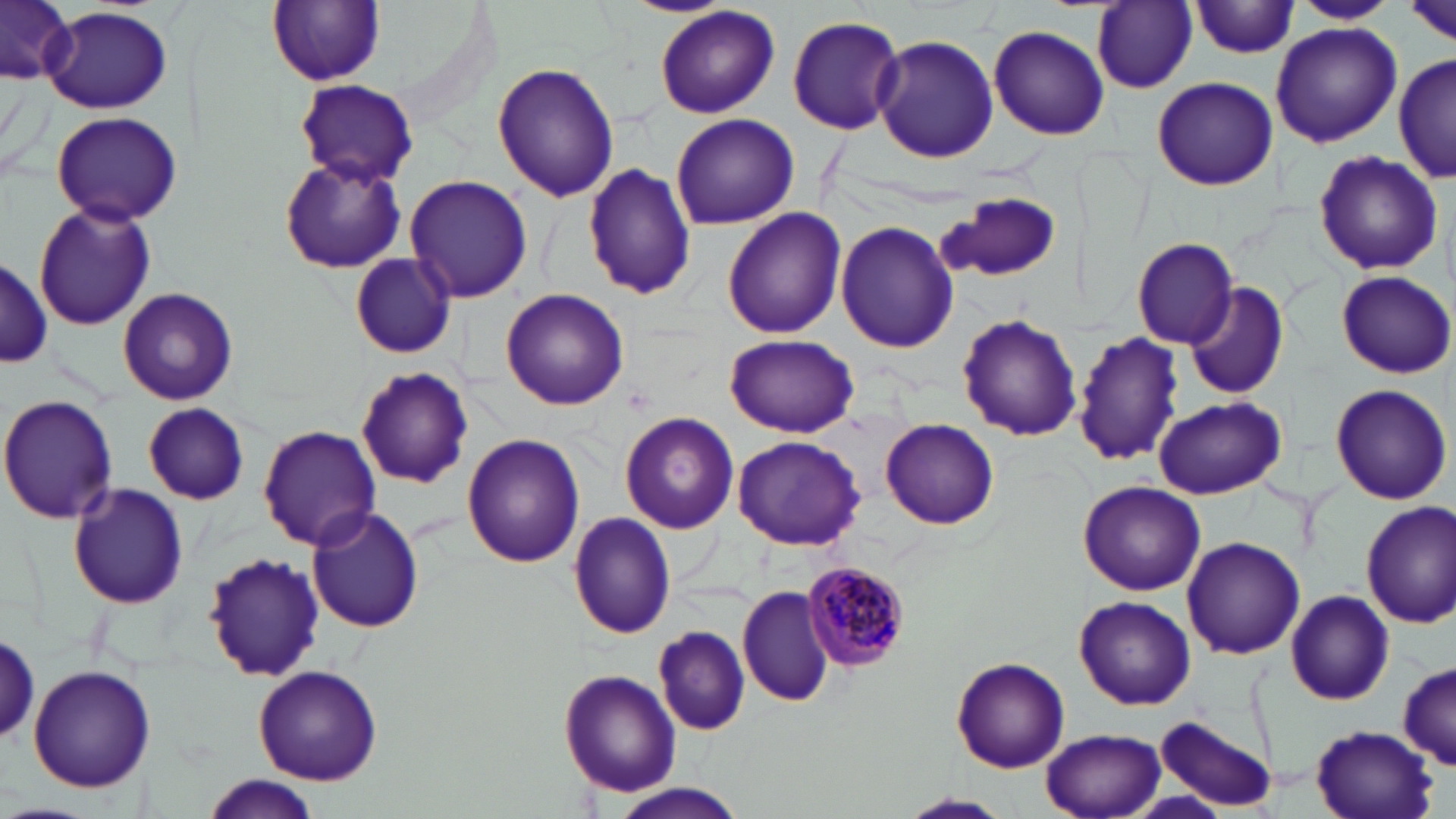

Approximate bounding boxes as (x1, y1, x2, y2) in pixels. Plasmodium malariae-infected red blood cell locations: (797, 562, 910, 673). Uninfected red blood cell locations: (2, 0, 77, 84), (264, 0, 389, 88), (1403, 0, 1455, 48), (1093, 1, 1198, 92), (1294, 1, 1395, 25), (1189, 3, 1303, 59), (39, 5, 174, 114), (654, 6, 780, 119), (787, 16, 904, 135), (1270, 22, 1401, 149), (988, 25, 1108, 139), (872, 34, 998, 163), (1393, 53, 1456, 186), (493, 61, 619, 201), (1150, 75, 1280, 191), (294, 79, 417, 188), (50, 111, 183, 225), (670, 113, 801, 229), (1313, 151, 1445, 275), (277, 156, 406, 273), (584, 163, 696, 302), (404, 174, 533, 303), (935, 192, 1062, 285), (33, 203, 157, 331), (721, 208, 848, 338), (836, 222, 958, 354), (1131, 237, 1239, 348), (348, 254, 456, 359), (0, 255, 50, 372), (1336, 270, 1454, 378), (1185, 279, 1290, 400), (118, 287, 238, 403), (500, 287, 629, 411), (956, 313, 1083, 441), (1072, 330, 1185, 470), (726, 333, 859, 436), (355, 367, 474, 488), (1329, 384, 1452, 505), (0, 393, 119, 525), (1154, 396, 1285, 499), (142, 403, 248, 505), (619, 411, 739, 534), (880, 418, 1000, 530), (258, 426, 380, 549), (462, 433, 584, 568), (733, 434, 866, 550), (1076, 481, 1205, 596), (69, 483, 188, 609), (1359, 502, 1456, 627), (306, 506, 424, 634), (568, 513, 678, 639), (1180, 536, 1306, 659), (202, 550, 328, 684), (737, 585, 837, 706), (1284, 589, 1394, 705), (1075, 596, 1196, 711), (653, 625, 750, 736), (0, 628, 43, 746), (951, 656, 1071, 773), (1396, 661, 1453, 771), (28, 662, 155, 792), (254, 664, 382, 785), (559, 669, 681, 796), (1156, 716, 1277, 812), (1308, 722, 1440, 819), (1039, 728, 1168, 819), (202, 778, 323, 818), (611, 784, 748, 818), (901, 793, 1012, 817). Slide-level diagnosis: Plasmodium malariae. Single field of view. May-Grünwald-Giemsa stain. Light microscopy. Captured at 1000x magnification. Image is 1456×819 pixels. Thin blood film.